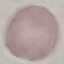
Summary:
  - Malaria status: uninfected
  - Capture: smartphone through the microscope eyepiece
  - Stain: Giemsa
  - Image type: cell patch, automatically extracted from a larger field of view and resized to 64 × 64 pixels
  - Preparation: thin blood smear